Report the malaria status of this cell.
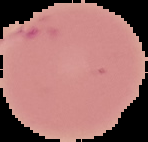

Uninfected.

{
  "image_type": "segmented cell region with the area outside set to black",
  "preparation": "thin blood film",
  "image_size": "148×142 pixels"
}